Outline every parasitised red blood cell.
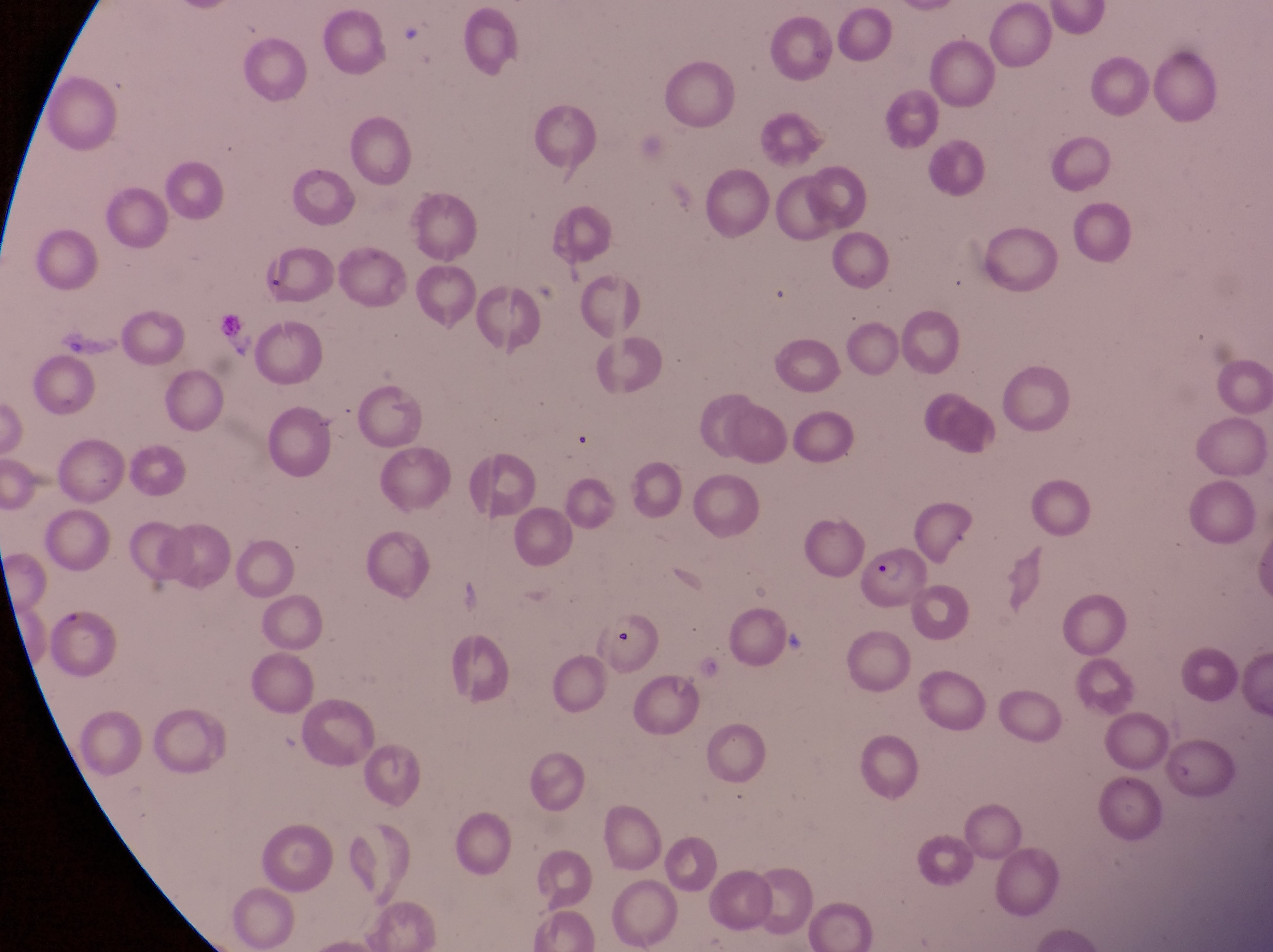
Approximate bounding boxes as [left, top, right, bottom] in pixels.
Parasitised red blood cells: [255, 242, 333, 302], [859, 547, 936, 614].

Summary:
  - Artifact (platelet-like body, stain precipitate, or debris) locations: [606, 631, 638, 656]
  - Image size: 1273×952 pixels
  - Magnification: 1000x
  - Capture: smartphone photograph through the eyepiece of an Olympus CX-23 microscope
  - Country: Uganda
  - Field of view: single
  - Preparation: thin blood smear